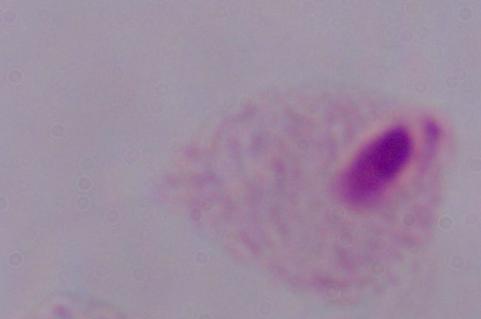

Summary:
  - Magnification: 1000x
  - Identification: trichomonad
  - Modality: photomicrograph